Assess this cell for malaria.
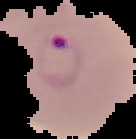

It is parasitized.

Image is 136×139 pixels. From a thin blood smear. Cell region segmented out of the field of view; the surrounding area is masked to black.